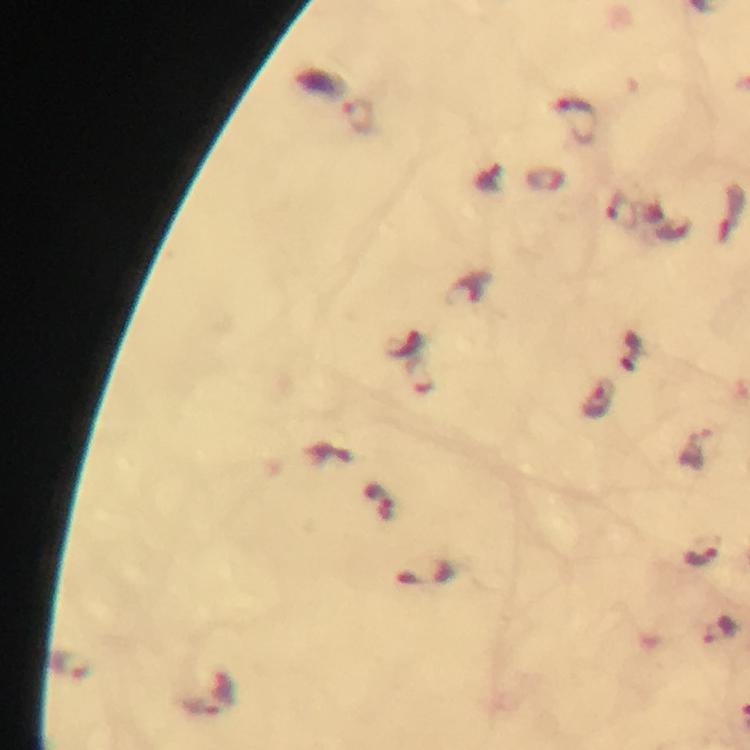
Approximate object centers, in pixels from the top-left corner.
Summary:
  - Malaria parasite locations: (x=360, y=116), (x=576, y=120), (x=419, y=375), (x=600, y=400), (x=377, y=495), (x=698, y=554), (x=719, y=630), (x=70, y=665)
  - Stain: Giemsa
  - Capture: smartphone camera through the microscope
  - Immersion oil: used
  - Context: from a malaria diagnostic workup
  - Magnification: 100x
  - Image size: 750×750 pixels
  - Cropped from: one field of view
  - Preparation: thick blood smear